Assess this cell for malaria.
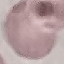

Uninfected.

Acquired by smartphone through the microscope eyepiece. Thin blood film. Giemsa-stained preparation. Cell patch, automatically extracted from a larger field of view and resized to 64 × 64 pixels.